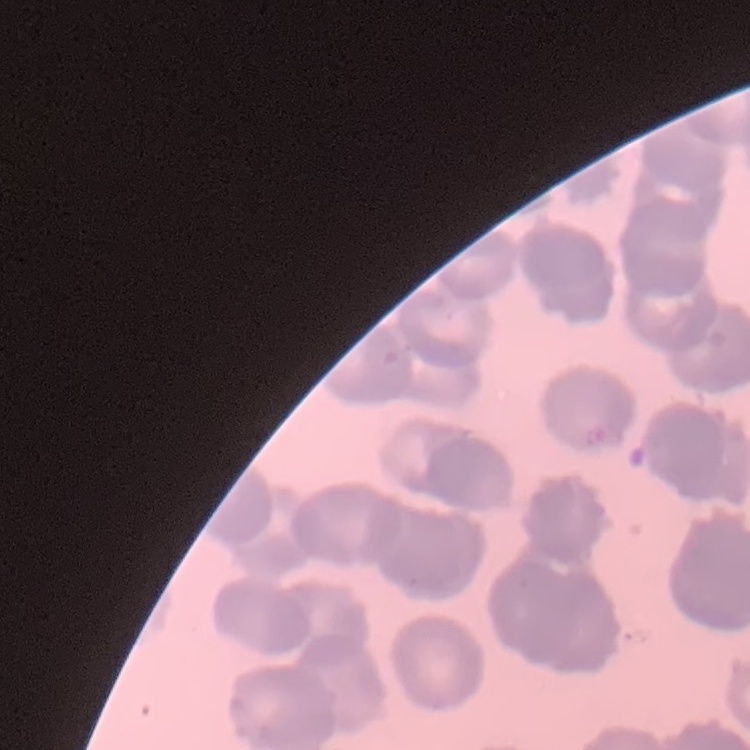
red_blood_cell_morphology: rouleaux formation
preparation: thin peripheral smear
image_type: one tile cut from a larger photomicrograph
stain: Field's or Giemsa